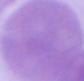
identification: erythrocyte
magnification: 1000x
modality: micrograph